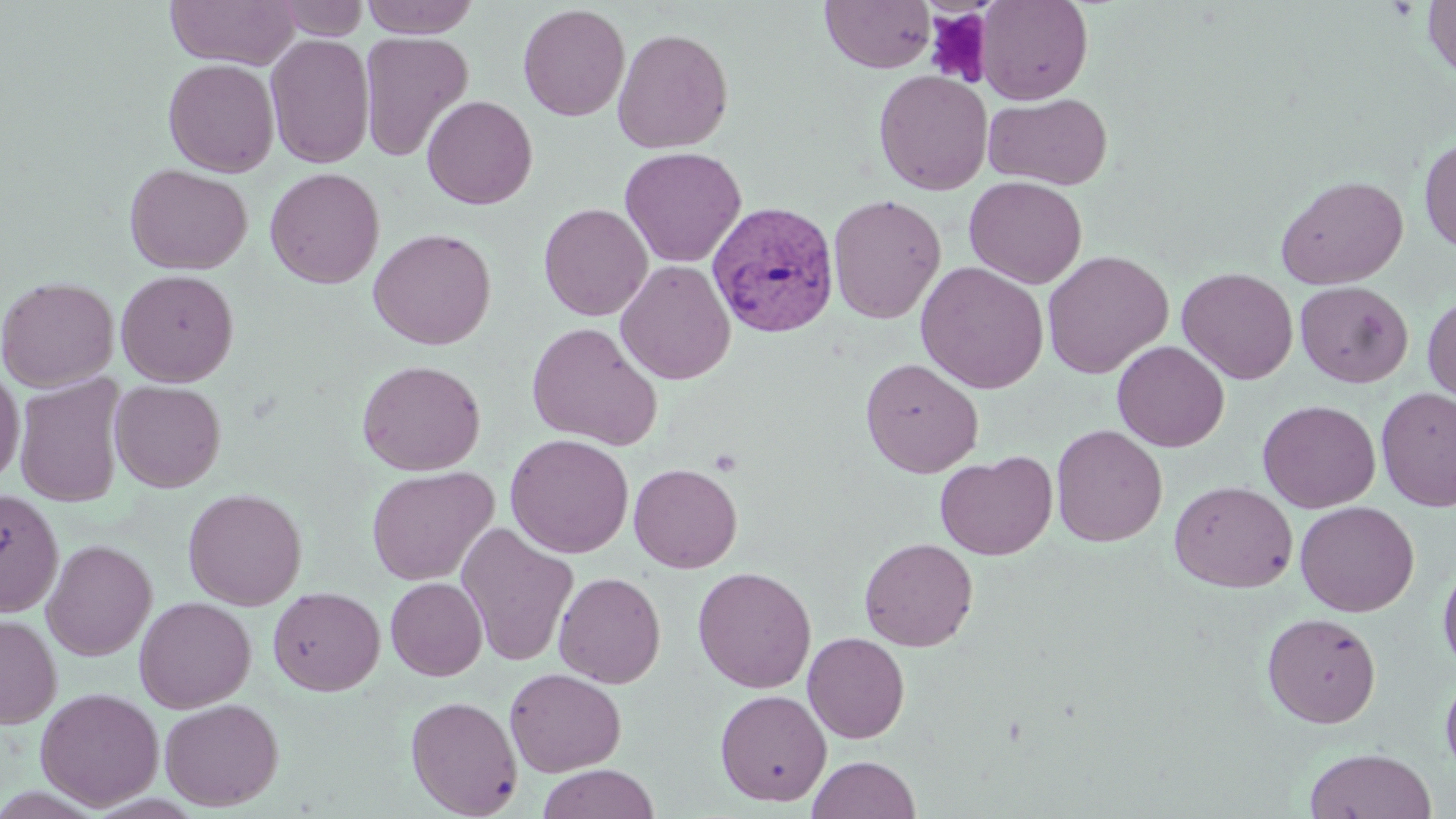

slide-level diagnosis = Plasmodium vivax
preparation = thin blood film
field of view = single
modality = optical microscopy
image size = 1456×819 pixels
Plasmodium vivax-infected red blood cell locations = approximate bounding boxes as [x1, y1, x2, y2] in pixels: [707, 200, 840, 339]
magnification = 1000x
platelet locations = approximate bounding boxes as [x1, y1, x2, y2] in pixels: [924, 8, 993, 87]
stain = May-Grünwald-Giemsa
uninfected red blood cell locations = approximate bounding boxes as [x1, y1, x2, y2] in pixels: [165, 0, 300, 69], [272, 0, 370, 40], [360, 0, 481, 37], [821, 0, 936, 73], [976, 0, 1093, 105], [1422, 1, 1456, 84], [517, 3, 630, 121], [612, 27, 734, 154], [359, 32, 474, 161], [264, 33, 375, 169], [163, 58, 279, 177], [874, 69, 993, 195], [983, 92, 1113, 190], [421, 95, 538, 210], [1418, 136, 1456, 253], [619, 146, 746, 267], [124, 163, 253, 274], [264, 167, 385, 289], [1275, 175, 1408, 289], [964, 176, 1088, 289], [827, 194, 946, 324], [538, 203, 653, 321], [368, 227, 497, 350], [1041, 250, 1174, 379], [615, 260, 736, 385], [915, 261, 1049, 394], [1177, 267, 1298, 384], [115, 268, 239, 387], [0, 276, 119, 392], [1295, 280, 1413, 388], [1422, 290, 1456, 406], [527, 321, 663, 450], [1112, 340, 1230, 452], [860, 357, 983, 477], [356, 359, 486, 476], [0, 365, 25, 486], [13, 374, 128, 508], [110, 380, 226, 492], [1376, 387, 1456, 511], [1257, 399, 1381, 513], [1050, 424, 1168, 546], [505, 433, 634, 558], [935, 452, 1058, 560], [629, 462, 742, 573], [366, 465, 498, 586], [1169, 480, 1297, 592], [0, 488, 64, 617], [183, 488, 307, 610], [1295, 501, 1419, 617], [456, 522, 579, 666], [859, 537, 978, 651], [41, 539, 157, 661], [1438, 560, 1456, 675], [693, 566, 816, 692], [553, 571, 666, 688], [385, 577, 488, 681], [267, 587, 384, 696], [134, 596, 256, 713], [1262, 612, 1381, 728], [0, 614, 61, 729], [803, 632, 910, 743], [505, 667, 626, 777], [1440, 672, 1456, 780], [35, 687, 164, 810], [715, 689, 832, 807], [405, 695, 523, 818], [159, 697, 284, 811], [1304, 747, 1436, 819], [807, 755, 919, 819], [537, 763, 660, 819]